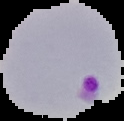
Image is 124×121 pixels. Malaria status: parasitized. From a thin blood smear. Cell region segmented out of the field of view; the surrounding area is masked to black.